Classify this cell by malaria status.
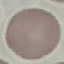

Uninfected.

Summary:
  - Stain: Giemsa
  - Image type: automatically extracted cell patch, resized to 64 × 64 pixels
  - Preparation: thin blood smear
  - Capture: smartphone camera at the microscope eyepiece